State the preparation type.
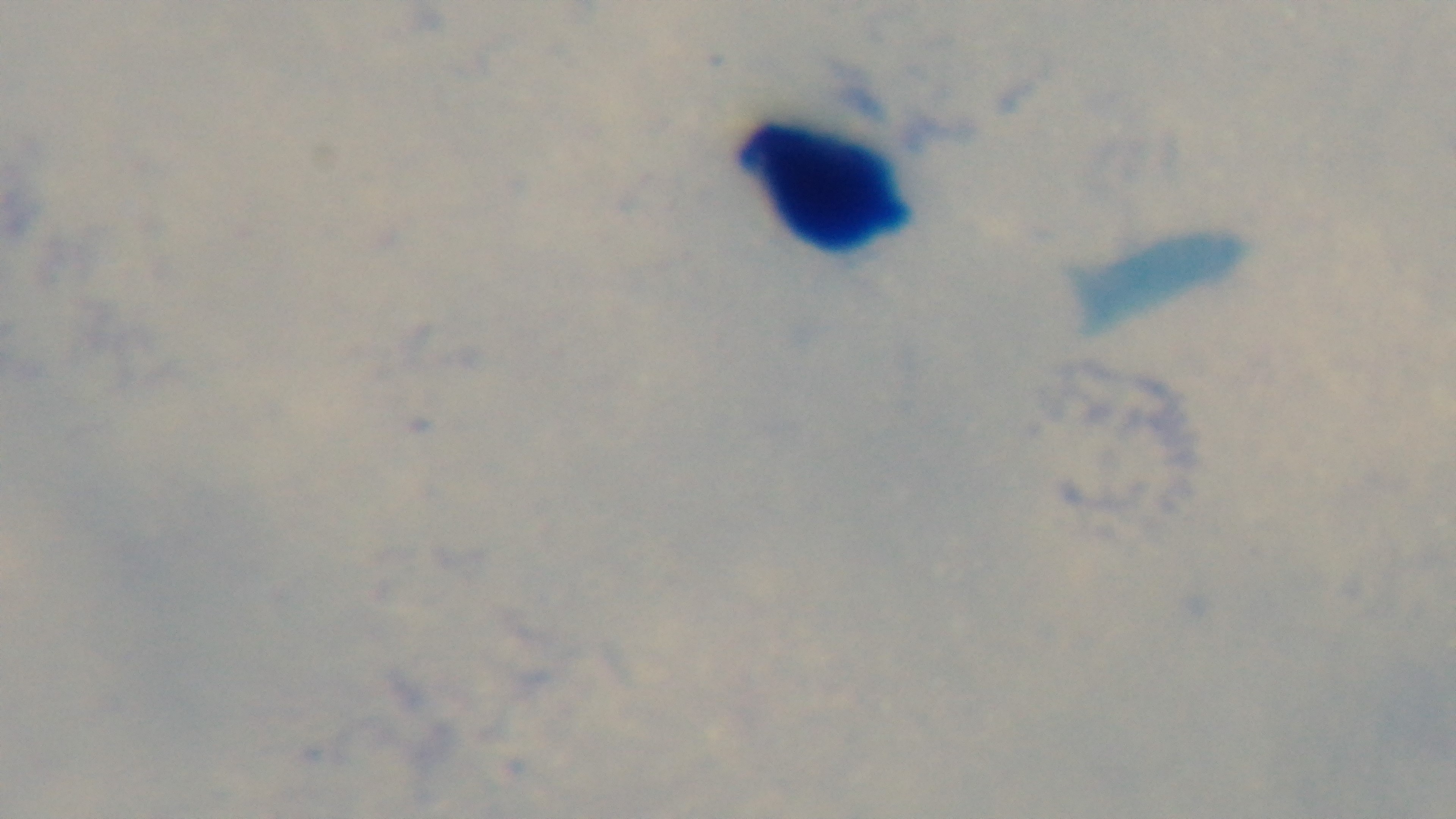

It is a thick blood film.

{
  "modality": "light microscopy",
  "objective": "100x oil immersion",
  "field_of_view": "one from the slide",
  "capture": "mounted 4K digital camera",
  "malaria_status": "negative",
  "stain": "Giemsa"
}